Assess for parasitized red blood cells.
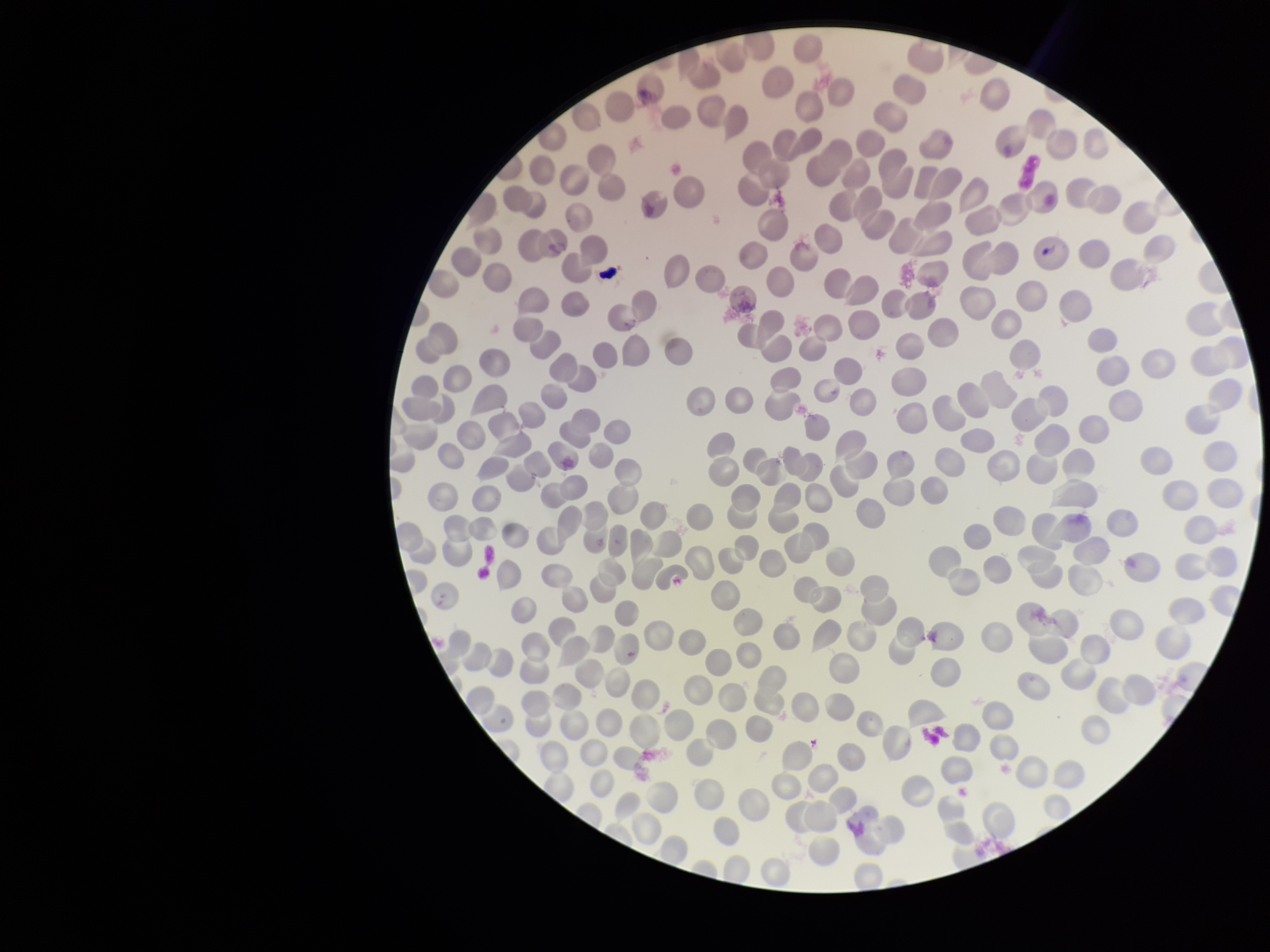

None detected.

{
  "red_blood_cell_count": 272,
  "parasitized_red_blood_cell_count": 0,
  "field_of_view": "one from this slide",
  "capture": "smartphone photograph through the microscope eyepiece",
  "patient_malaria_status": "negative",
  "preparation": "thin",
  "stain": "Giemsa",
  "image_size": "1270×952 pixels"
}